Describe the morphology of the erythrocytes.
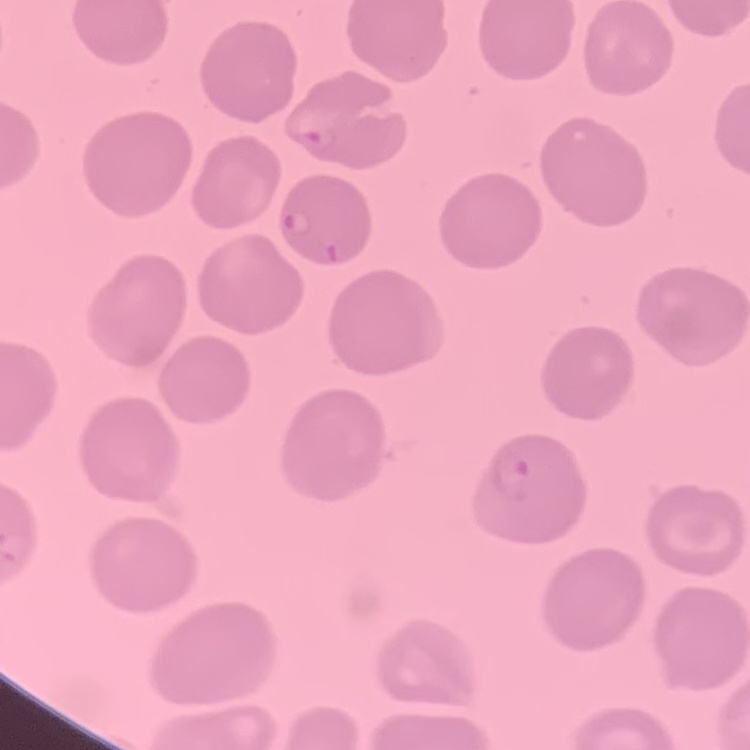

No rouleaux formation.

Summary:
  - Preparation: thin blood film
  - Image type: square crop of a larger photomicrograph
  - Stain: Field's or Giemsa